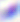
{
  "identification": "Toxoplasma gondii",
  "magnification": "400x",
  "modality": "micrograph"
}